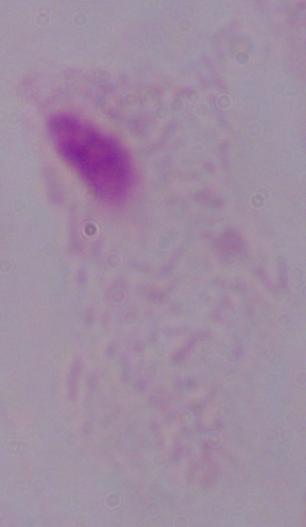
modality = photomicrograph
identification = trichomonad
magnification = 1000x